Assess the morphology of the erythrocytes.
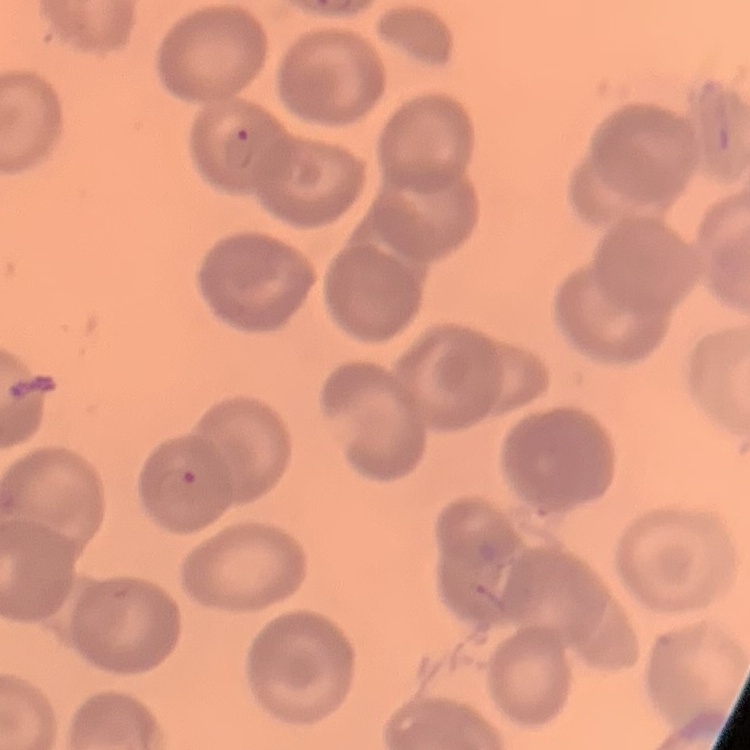

No rouleaux formation.

preparation: thin blood film
image_type: one tile cut from a larger photomicrograph
stain: Field's or Giemsa